Report the malaria status of this cell.
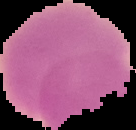

Uninfected.

Segmented cell region on a black background. Image is 136×130 pixels. From a thin blood film.